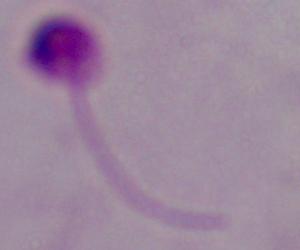

magnification = 1000x
modality = micrograph
identification = Leishmania